Classify this cell by malaria status.
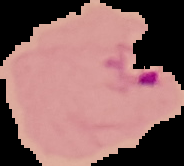
Parasitized.

Segmented cell region on a black background. From a thin blood smear. Image is 184×166 pixels.